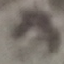

malaria status = uninfected
capture = smartphone camera at the microscope eyepiece
preparation = thin blood film
stain = Giemsa
image type = automatically extracted cell patch, resized to 64 × 64 pixels